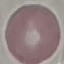

malaria status = uninfected
capture = smartphone camera at the microscope eyepiece
preparation = thin blood smear
stain = Giemsa
image type = cell patch, automatically extracted from a larger field of view and resized to 64 × 64 pixels